Describe the morphology of the erythrocytes.
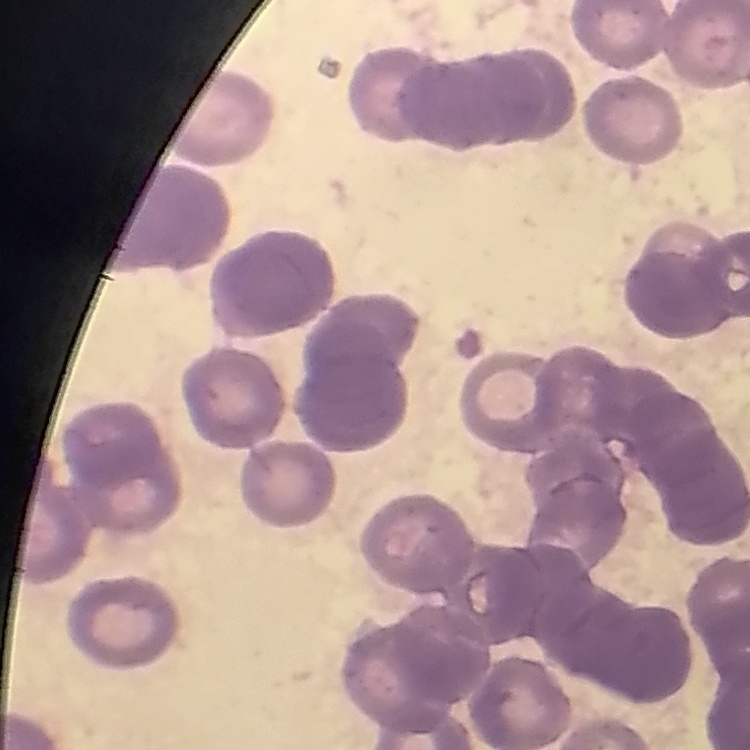

Rouleaux formation.

stain = Field's or Giemsa
preparation = thin blood film
image type = square crop of a larger photomicrograph